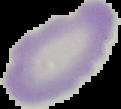

image type = cell region segmented out of the field of view; surrounding area masked to black
image size = 121×109 pixels
preparation = thin blood smear
result = no Plasmodium parasites seen